Assess the morphology of the red blood cells.
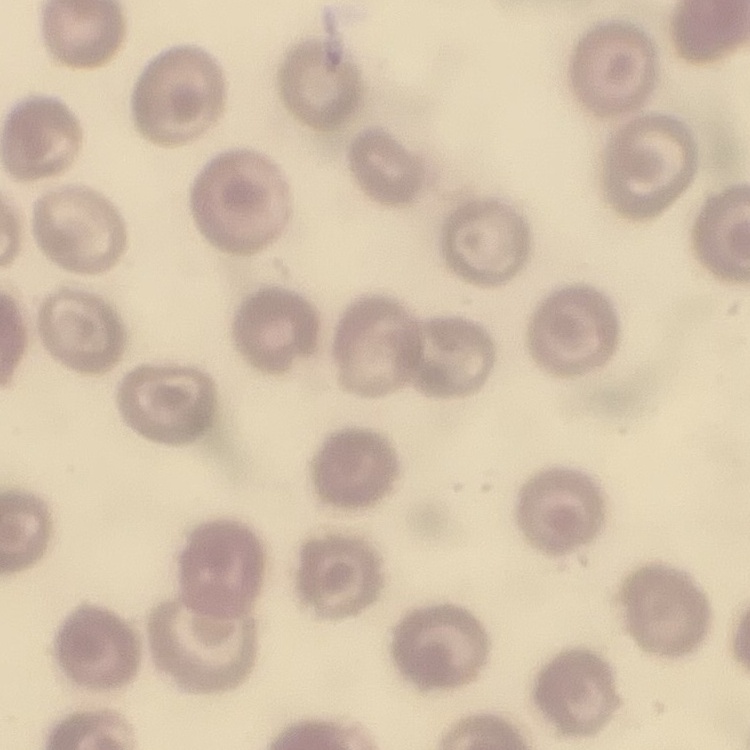

They show no rouleaux formation.

Summary:
  - Preparation: thin blood film
  - Image type: square crop of a larger photomicrograph
  - Stain: Field's or Giemsa